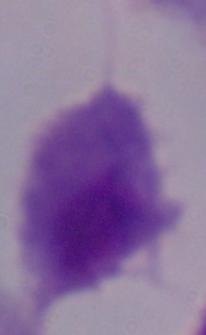
Summary:
  - Magnification: 1000x
  - Identification: trichomonad
  - Modality: micrograph